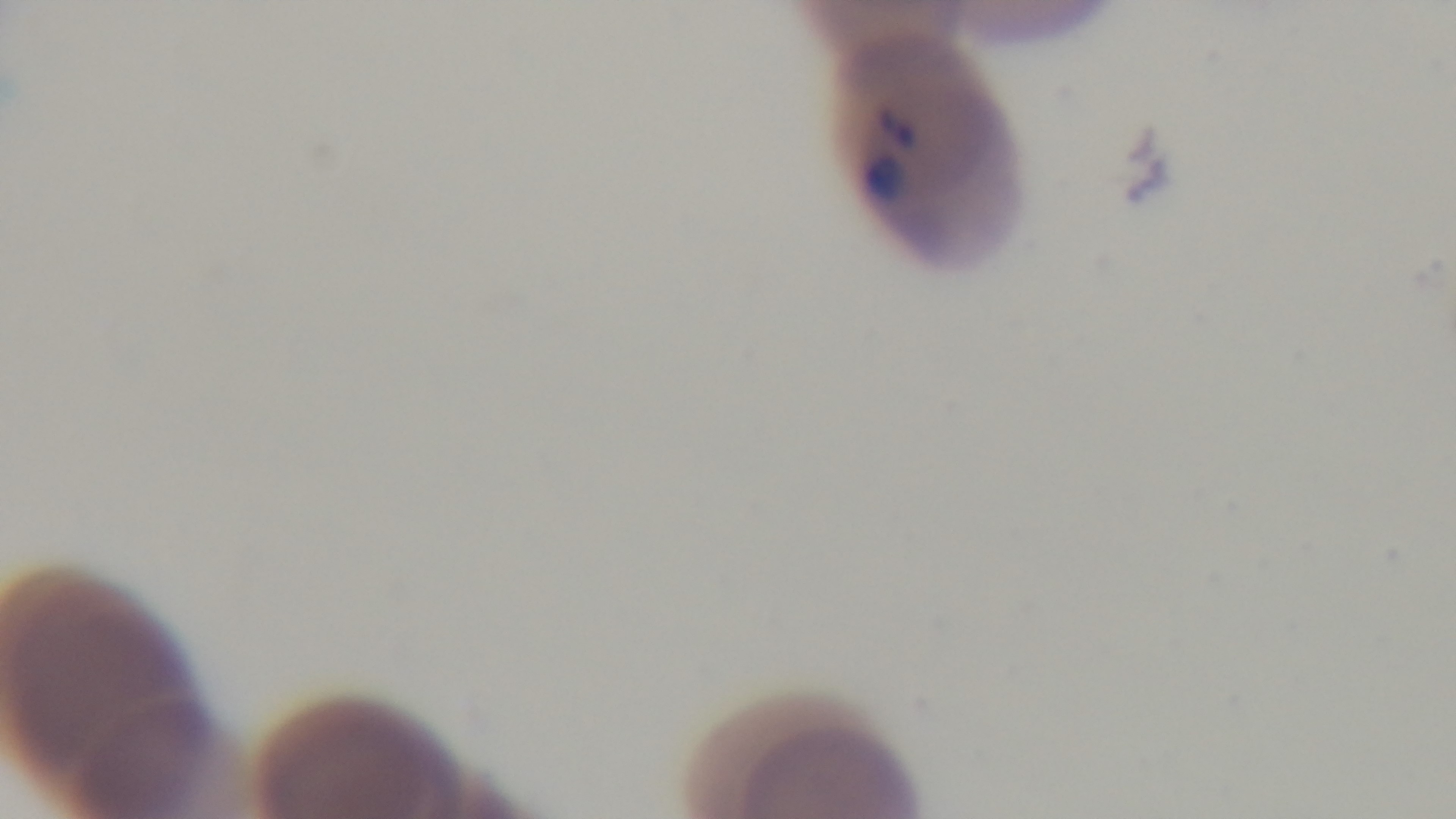

capture = mounted 4K digital camera
modality = light microscopy
objective = 100x oil immersion
stain = Giemsa
field of view = one from the slide
preparation = thin smear
malaria status = positive